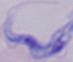
Micrograph. A trypanosome is shown. 1000x magnification.